State the preparation type.
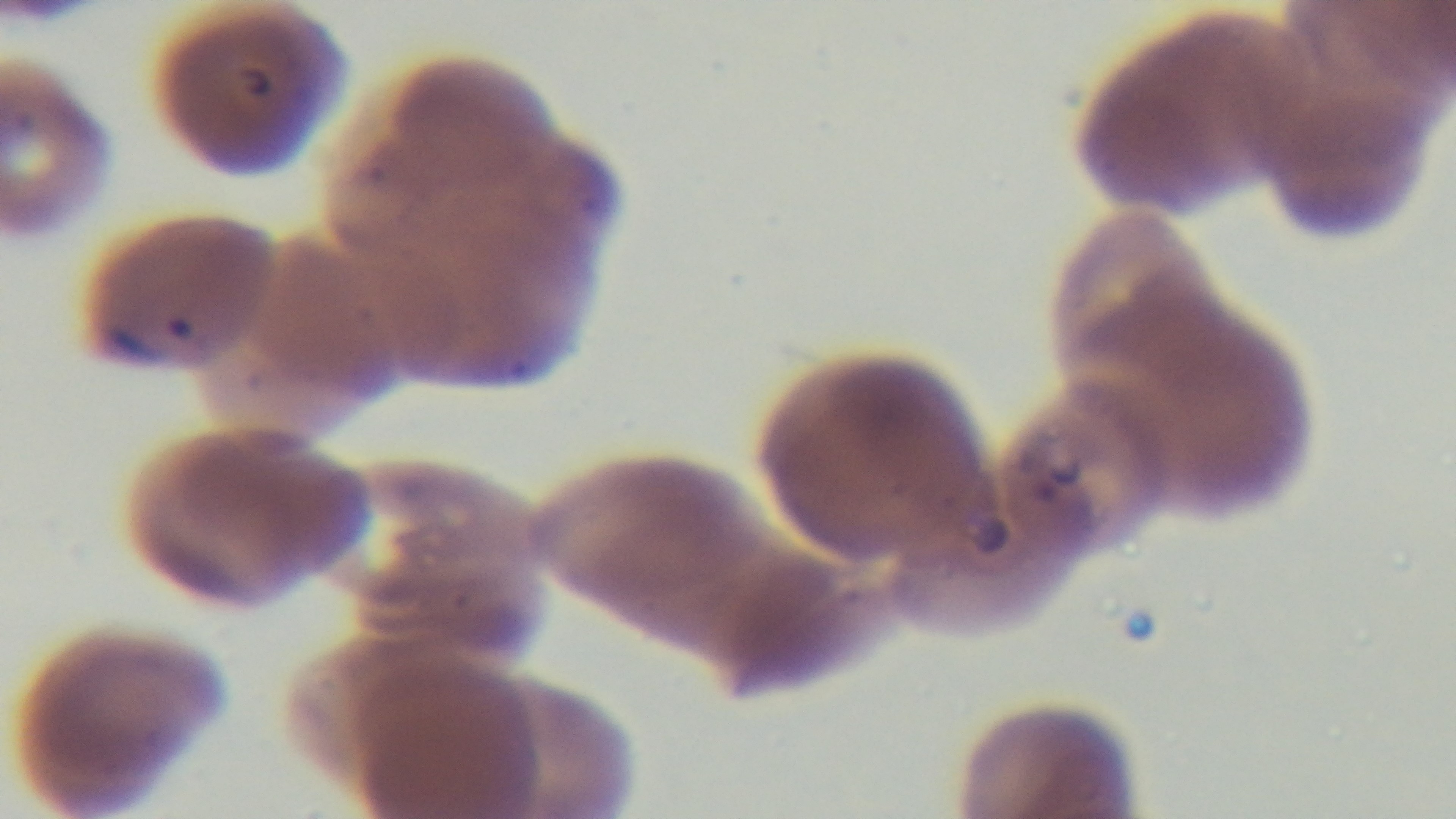

A thin smear.

modality: light microscopy
capture: mounted 4K digital camera
stain: Giemsa
field_of_view: one from the slide
malaria_status: positive
objective: 100x oil immersion